Comment on the morphology of the erythrocytes.
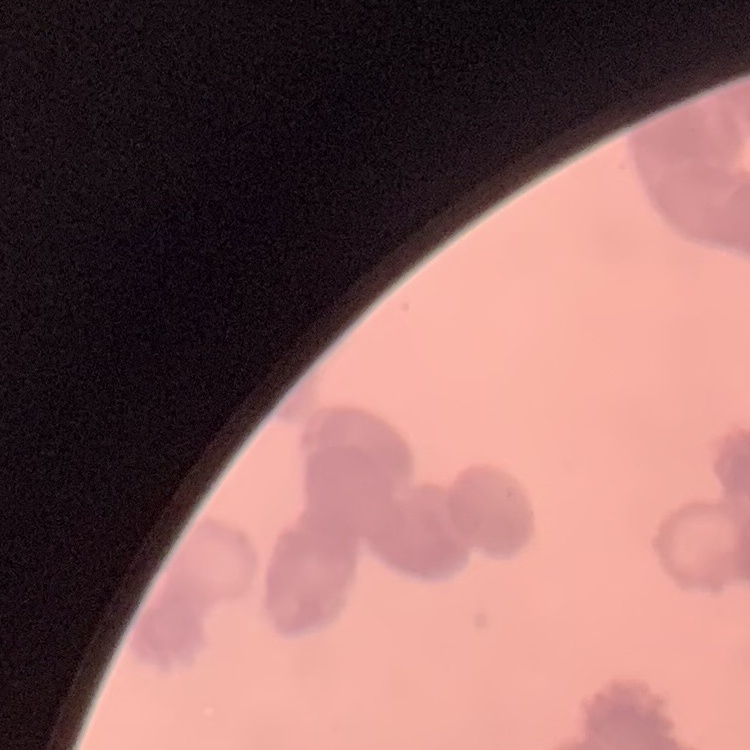
They show rouleaux formation.

image type = square crop of a larger photomicrograph
preparation = thin peripheral smear
stain = Field's or Giemsa